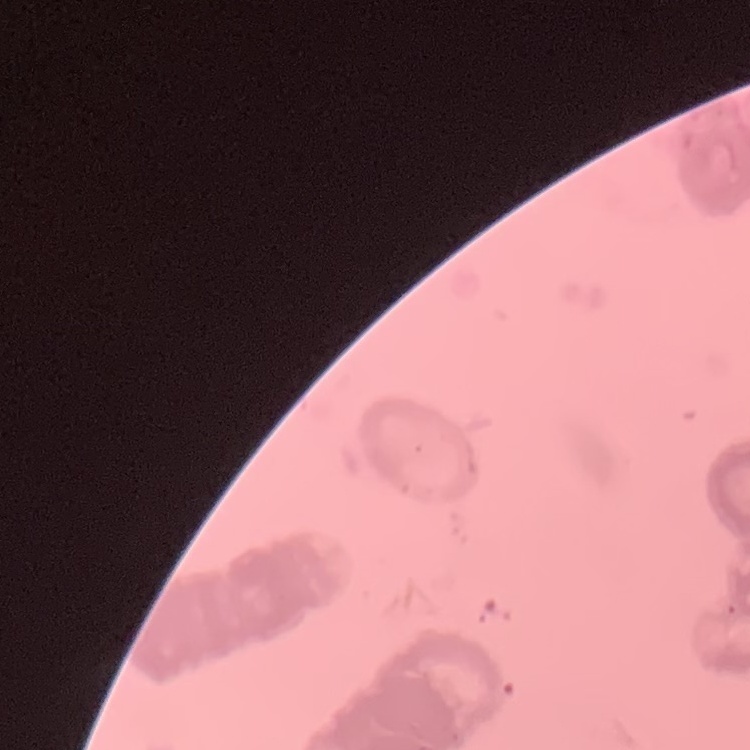

red blood cell morphology = rouleaux formation
stain = Field's or Giemsa
preparation = thin peripheral smear
image type = square crop of a larger photomicrograph